Outline each blood parasite and name the species.
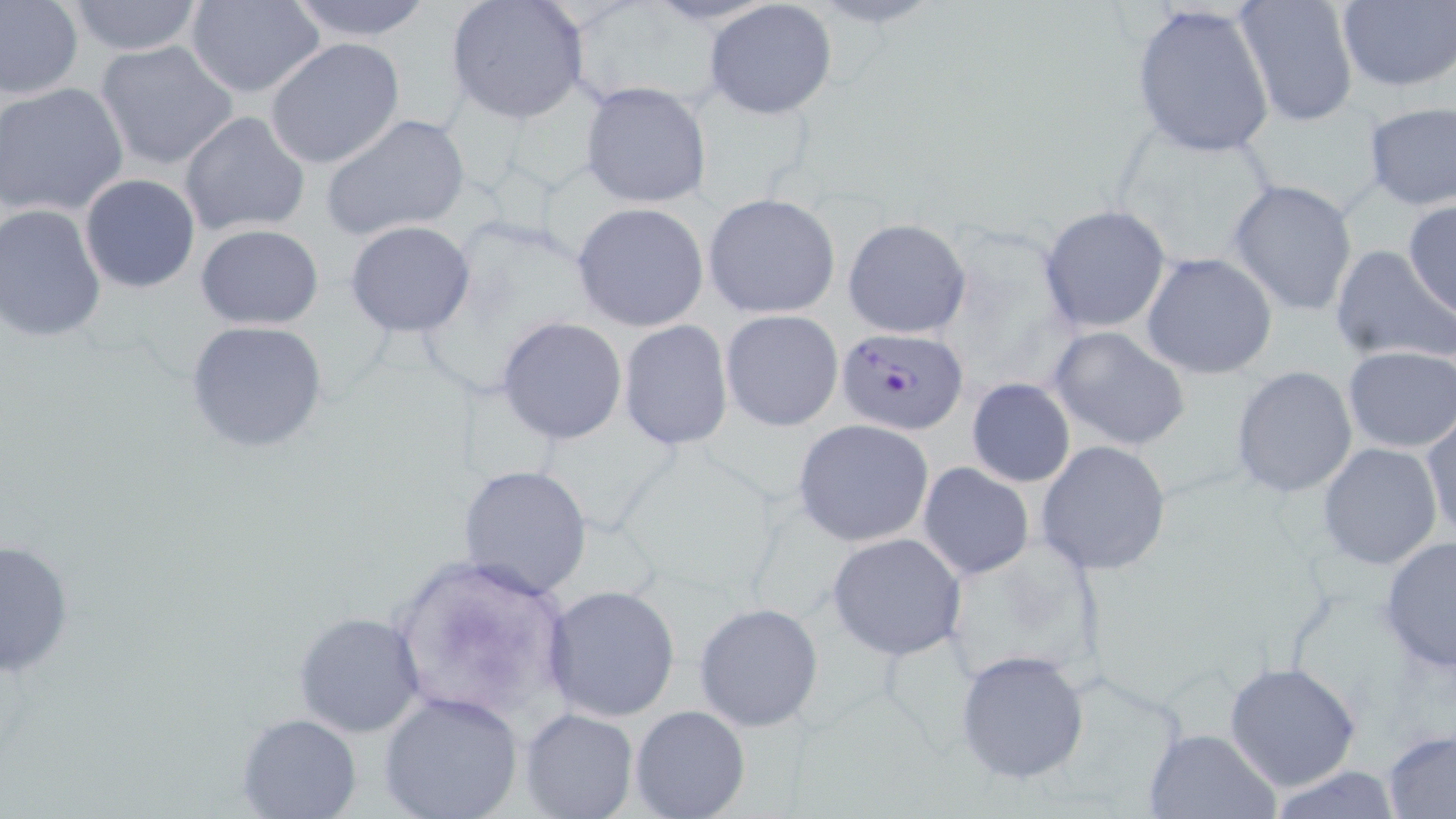
Approximate bounding boxes as [x1, y1, x2, y2] in pixels.
Plasmodium falciparum-infected red blood cells: [832, 328, 968, 435].
No Plasmodium ovale, Plasmodium malariae, Plasmodium vivax, Babesia divergens, or Trypanosoma brucei observed.

Uninfected red blood cell locations: [0, 0, 84, 102], [62, 0, 208, 56], [283, 0, 440, 42], [444, 0, 589, 125], [1231, 0, 1359, 126], [185, 1, 325, 100], [703, 1, 839, 120], [1335, 1, 1456, 92], [1130, 4, 1274, 158], [94, 39, 241, 171], [264, 39, 407, 170], [579, 80, 714, 208], [0, 82, 130, 218], [1362, 102, 1456, 211], [180, 111, 312, 236], [320, 112, 470, 241], [79, 174, 201, 293], [1227, 179, 1359, 317], [703, 193, 841, 318], [1402, 200, 1456, 320], [572, 201, 710, 331], [0, 203, 107, 343], [1039, 204, 1171, 333], [843, 218, 971, 338], [344, 221, 476, 336], [194, 224, 324, 330], [1329, 243, 1451, 366], [1140, 253, 1279, 377], [720, 309, 843, 431], [497, 316, 627, 445], [185, 318, 330, 454], [618, 320, 734, 451], [1048, 327, 1190, 452], [1341, 346, 1454, 453], [1231, 366, 1359, 500], [966, 378, 1075, 488], [1422, 412, 1455, 545], [792, 419, 935, 547], [1034, 440, 1171, 576], [1317, 441, 1444, 571], [918, 462, 1034, 580], [458, 463, 593, 600], [827, 532, 967, 660], [1, 535, 75, 677], [1378, 535, 1456, 672], [542, 584, 681, 723], [694, 601, 824, 732], [293, 611, 425, 738], [954, 648, 1090, 786], [1224, 660, 1365, 793], [378, 690, 524, 819], [629, 705, 750, 819], [520, 709, 637, 819], [236, 711, 362, 818], [1143, 727, 1280, 818], [1384, 730, 1455, 818], [1262, 765, 1404, 818]. Slide-level diagnosis: Plasmodium falciparum. Captured at 1000x magnification. Single field of view. Thin blood film. May-Grünwald-Giemsa-stained preparation. Image is 1456×819 pixels. Optical microscopy.